Report the malaria status of this cell.
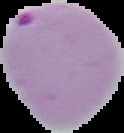

It is parasitized.

Summary:
  - Image type: segmented cell region with the area outside set to black
  - Preparation: thin blood smear
  - Image size: 124×133 pixels